Classify this cell by malaria status.
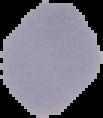

It is uninfected.

Segmented cell region on a black background. From a thin blood film. Image is 103×118 pixels.